Give the preparation type.
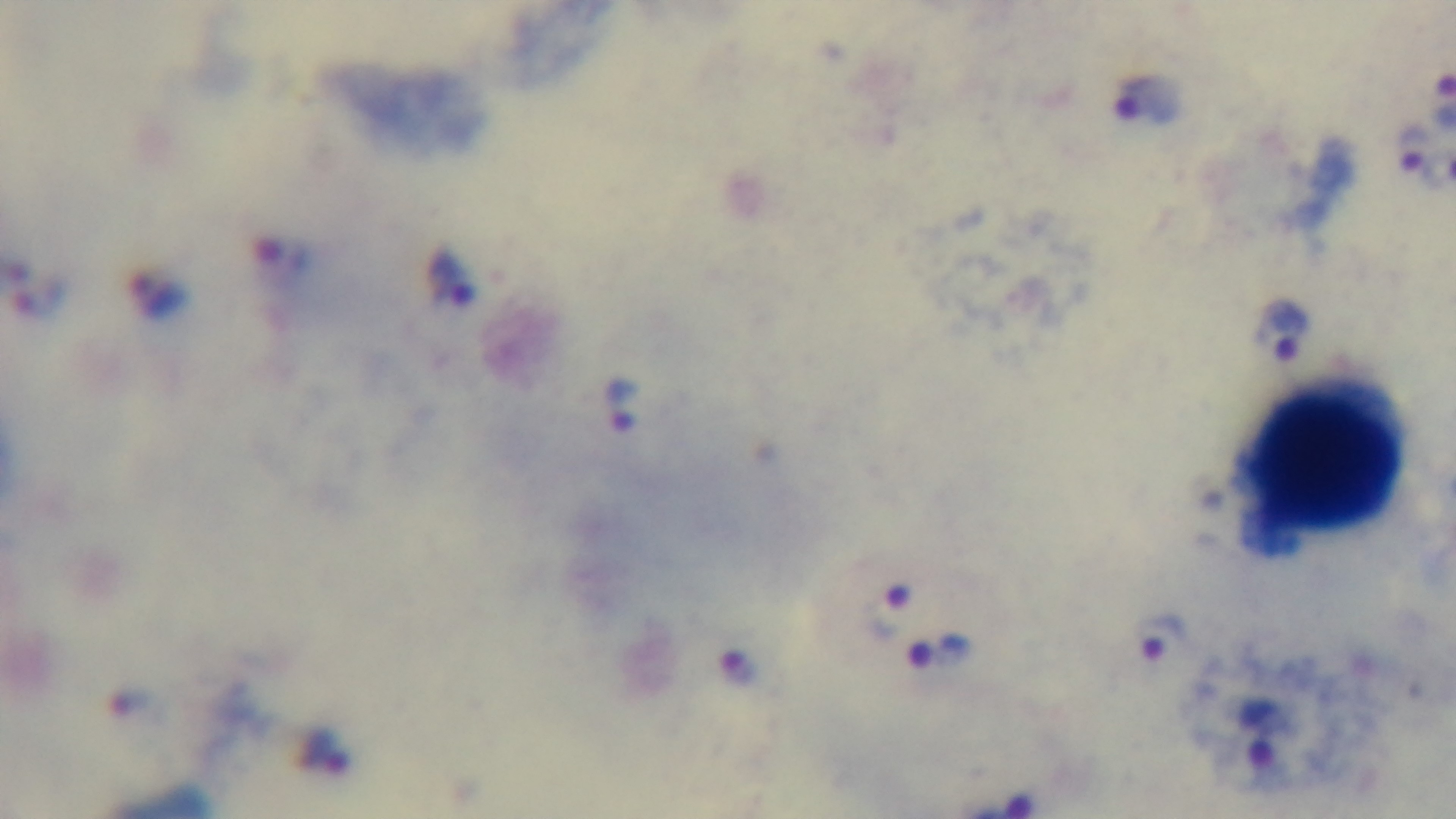
It is a thick blood film.

Summary:
  - Field of view: one from the slide
  - Malaria status: infected
  - Capture: mounted 4K digital camera
  - Stain: Giemsa
  - Objective: 100x oil immersion
  - Modality: light microscopy